Assess this cell for malaria.
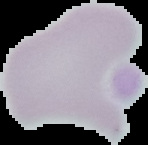

Uninfected.

Image is 148×145 pixels. From a thin blood smear. The area outside the segmented cell region is set to black.